Locate every malaria parasite.
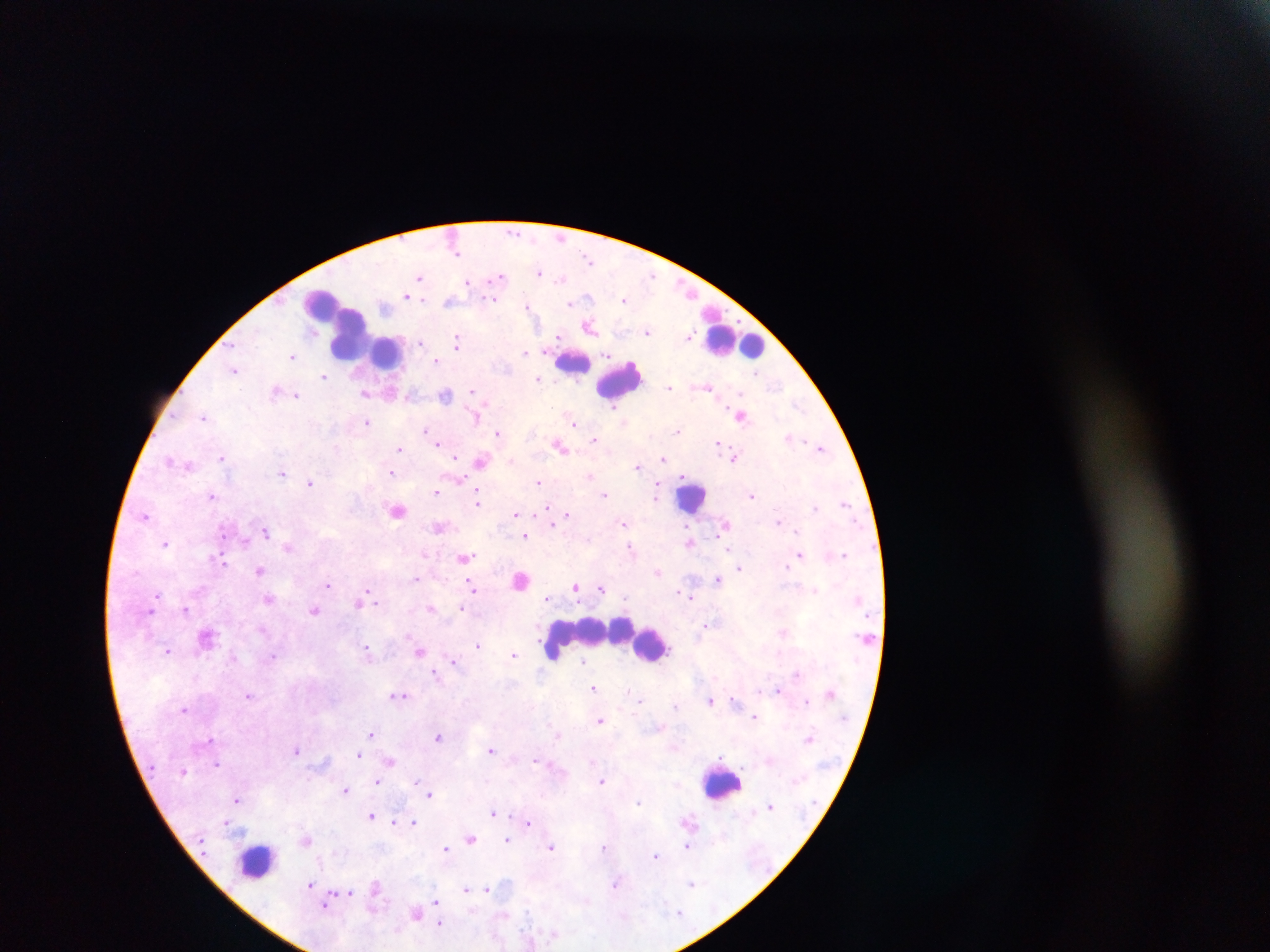

Approximate centers as {x, y} in pixels.
Malaria parasites: {513, 231}, {456, 253}, {588, 258}, {540, 273}, {652, 275}, {499, 276}, {420, 277}, {561, 279}, {469, 282}, {407, 295}, {587, 297}, {493, 300}, {625, 300}, {448, 301}, {571, 304}, {527, 305}, {589, 327}, {648, 331}, {559, 336}, {690, 336}, {421, 342}, {457, 342}, {525, 352}, {608, 354}, {293, 356}, {436, 360}, {234, 370}, {757, 373}, {323, 376}, {538, 379}, {669, 387}, {707, 387}, {276, 391}, {471, 391}, {391, 392}, {366, 393}, {296, 395}, {445, 395}, {798, 404}, {615, 406}, {740, 416}, {204, 417}, {476, 417}, {366, 422}, {574, 422}, {426, 430}, {678, 431}, {498, 433}, {791, 438}, {594, 439}, {438, 442}, {717, 442}, {560, 446}, {821, 448}, {399, 449}, {456, 457}, {733, 457}, {221, 458}, {664, 459}, {170, 460}, {481, 461}, {637, 467}, {282, 473}, {392, 474}, {590, 476}, {461, 480}, {538, 481}, {311, 482}, {658, 489}, {436, 492}, {604, 494}, {213, 495}, {752, 495}, {656, 496}, {478, 500}, {845, 503}, {546, 507}, {814, 507}, {397, 511}, {515, 514}, {567, 515}, {145, 516}, {778, 521}, {552, 524}, {623, 524}, {439, 527}, {222, 531}, {266, 531}, {797, 531}, {525, 536}, {245, 541}, {690, 542}, {165, 544}, {287, 547}, {630, 547}, {729, 550}, {844, 554}, {800, 555}, {465, 558}, {221, 560}, {786, 566}, {739, 568}, {260, 570}, {658, 572}, {415, 579}, {717, 579}, {521, 580}, {328, 584}, {472, 587}, {576, 587}, {601, 589}, {816, 590}, {158, 595}, {685, 595}, {690, 596}, {364, 597}, {547, 598}, {269, 599}, {359, 601}, {373, 601}, {431, 608}, {462, 608}, {186, 609}, {314, 610}, {707, 625}, {783, 632}, {477, 645}, {367, 649}, {168, 651}, {420, 652}, {514, 654}, {272, 656}, {455, 661}, {583, 661}, {435, 673}, {795, 674}, {594, 687}, {778, 690}, {400, 695}, {248, 696}, {734, 699}, {641, 701}, {710, 701}, {806, 701}, {675, 706}, {184, 709}, {754, 717}, {600, 720}, {371, 734}, {557, 735}, {438, 736}, {809, 738}, {296, 749}, {491, 749}, {358, 754}, {721, 756}, {535, 759}, {390, 762}, {593, 762}, {217, 765}, {602, 780}, {378, 781}, {417, 782}, {346, 790}, {430, 794}, {238, 799}, {638, 803}, {770, 805}, {493, 812}, {371, 815}, {226, 822}, {414, 822}, {529, 822}, {394, 823}, {470, 839}, {507, 839}, {306, 840}, {552, 846}, {687, 846}, {603, 847}, {445, 848}, {656, 856}, {691, 883}, {615, 884}, {310, 885}, {375, 887}, {465, 889}, {486, 889}, {349, 892}, {436, 901}, {326, 904}, {679, 912}, {416, 913}, {440, 924}.

Leukocyte locations: {350, 329}, {735, 341}, {387, 352}, {572, 363}, {621, 380}, {692, 497}, {591, 635}, {651, 643}, {553, 651}, {722, 783}, {257, 862}. Sample from Ghana. One field of view. Mobile-phone photograph taken through the microscope. Image is 1270×952 pixels. Thick blood film.